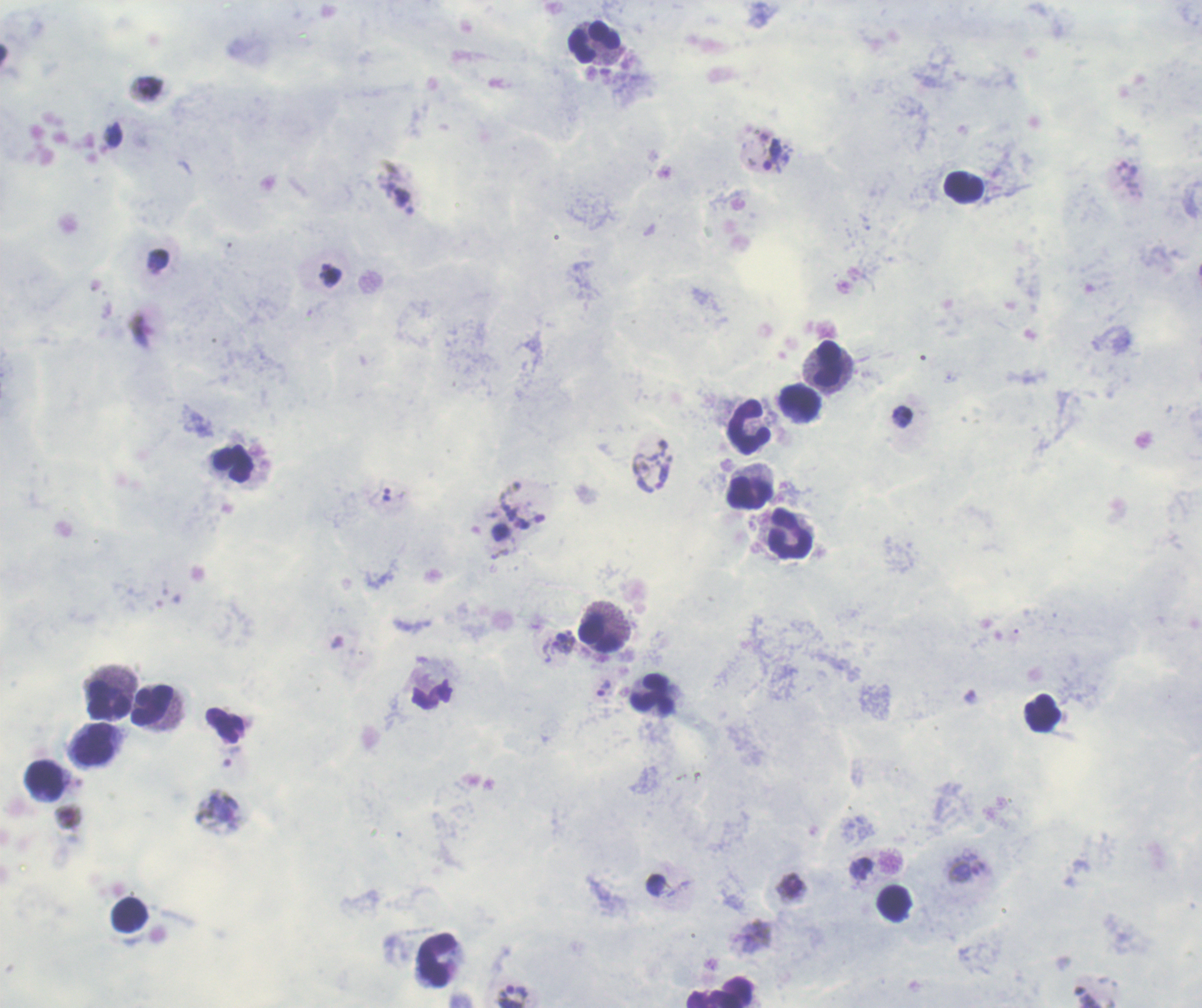
{
  "result": "Plasmodium parasites identified",
  "leukocyte_locations": "approximate centers as {x, y} in pixels: {594, 44}, {964, 187}, {828, 363}, {800, 403}, {749, 428}, {233, 466}, {749, 493}, {790, 535}, {598, 634}, {653, 695}, {108, 701}, {152, 705}, {1043, 713}, {94, 745}, {46, 780}, {437, 960}",
  "coloration_quality": "good",
  "image_size": "1202×1008 pixels",
  "stain": "Romanowsky",
  "context": "previously used in an actual diagnosis",
  "trophozoite_locations": "approximate centers as {x, y} in pixels: {772, 154}, {386, 495}, {564, 643}, {604, 688}, {517, 992}",
  "magnification": "100x",
  "field_of_view": "one from this slide",
  "background_quality": "unsatisfactory",
  "preparation": "thick smear of blood"
}